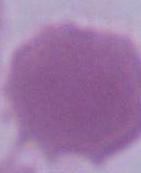

identification = erythrocyte
magnification = 1000x
modality = micrograph